Report the malaria status of this cell.
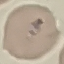

Uninfected.

image type = automatically extracted cell patch, resized to 64 × 64 pixels
capture = smartphone through the microscope eyepiece
preparation = thin blood smear
stain = Giemsa